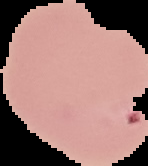
preparation: thin blood film
image_type: segmented cell region on a black background
result: no malaria parasites seen
image_size: 148×166 pixels